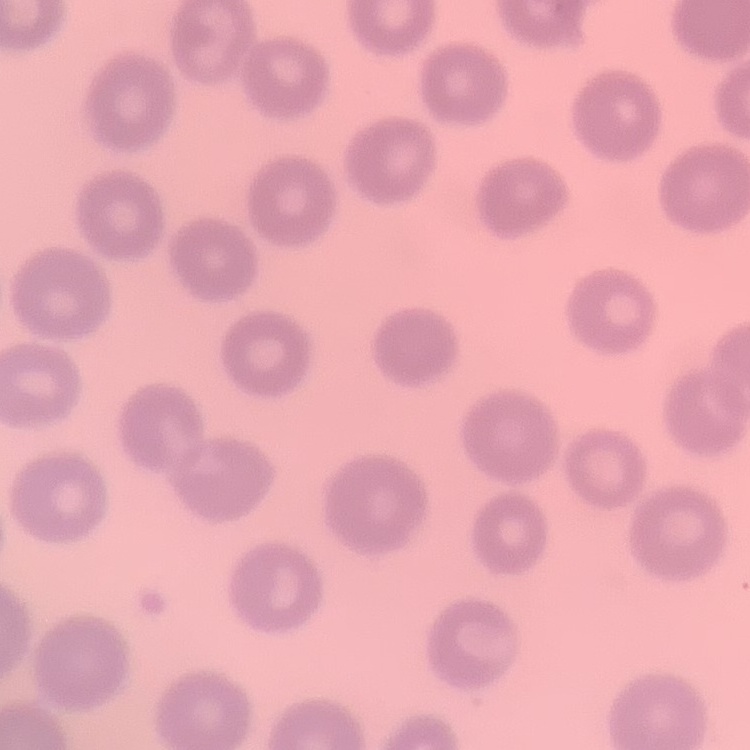
{
  "red_blood_cell_morphology": "no rouleaux formation",
  "stain": "Field's or Giemsa",
  "preparation": "thin blood film",
  "image_type": "square crop of a larger photomicrograph"
}